Report the malaria status of this cell.
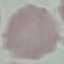
Uninfected.

Thin blood smear. Automatically extracted cell patch, resized to 64 × 64 pixels. Giemsa stain. Photographed with a smartphone camera at the microscope eyepiece.